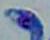
Captured at 1000x magnification. Photomicrograph. Toxoplasma gondii is shown.